Outline each Plasmodium falciparum-infected red blood cell.
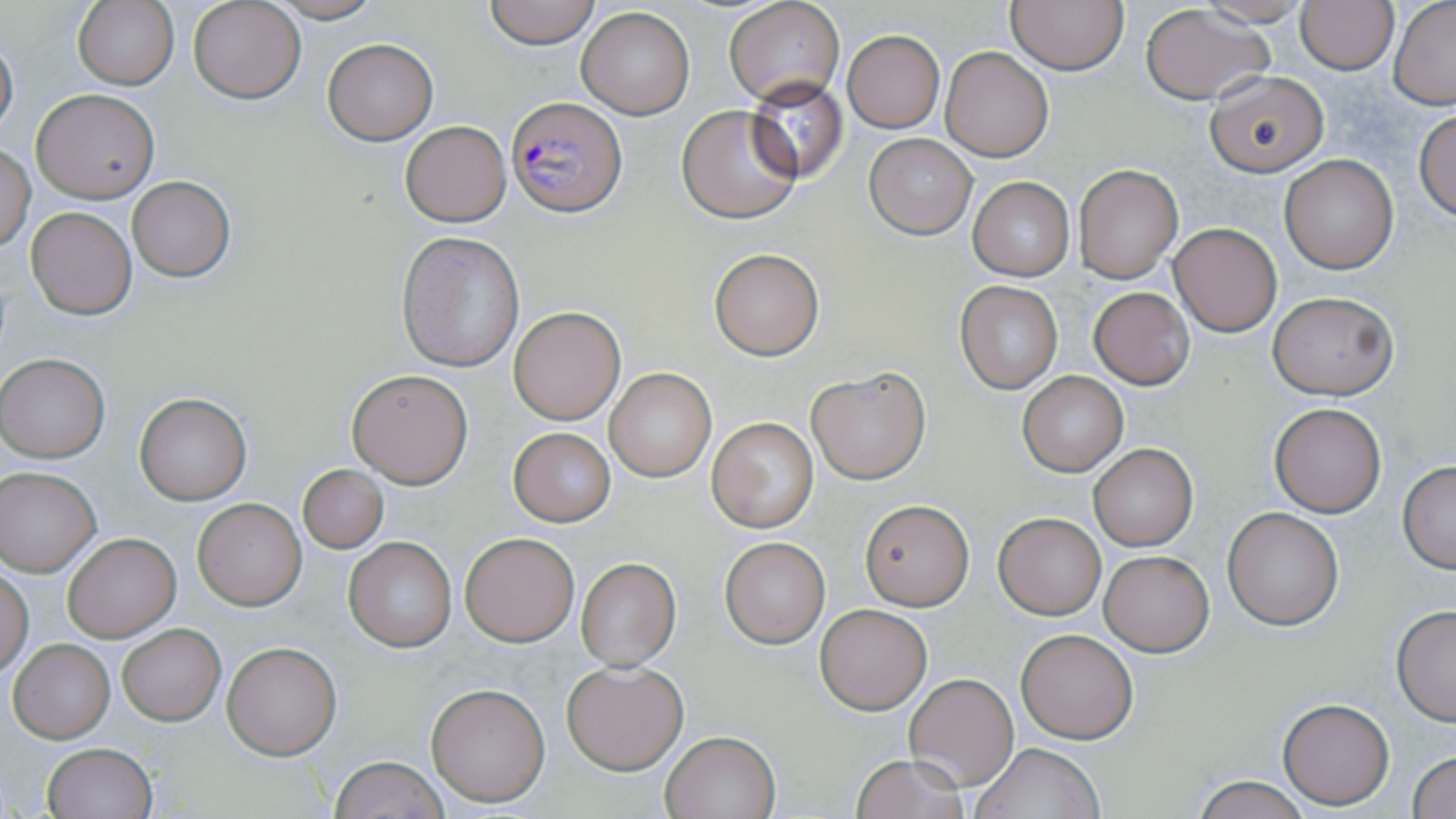

Approximate bounding boxes as (x1,y1)-(x2,y2) corner pairs in pixels.
Plasmodium falciparum-infected red blood cells: (508,96)-(627,217).

Uninfected red blood cell locations: (188,0)-(306,103), (264,0)-(386,23), (484,0)-(600,48), (73,1)-(178,89), (725,1)-(844,106), (1007,1)-(1128,74), (1195,1)-(1313,26), (1295,1)-(1398,74), (1388,1)-(1456,108), (1139,4)-(1274,105), (577,7)-(695,119), (0,31)-(17,137), (842,31)-(945,132), (322,38)-(437,145), (940,46)-(1052,161), (1203,71)-(1331,178), (745,77)-(847,183), (31,89)-(160,202), (677,105)-(801,223), (1414,109)-(1456,221), (400,120)-(511,226), (864,133)-(976,238), (0,145)-(35,253), (1280,155)-(1399,273), (1073,165)-(1183,282), (127,177)-(236,281), (968,177)-(1075,281), (25,207)-(137,320), (1170,223)-(1282,337), (397,232)-(527,373), (709,247)-(824,360), (954,280)-(1065,395), (1089,287)-(1194,388), (1267,290)-(1398,400), (508,307)-(626,425), (1,354)-(109,462), (806,367)-(930,485), (346,368)-(473,488), (605,369)-(716,481), (1018,370)-(1128,475), (134,393)-(251,504), (1269,402)-(1386,517), (706,417)-(818,534), (508,428)-(615,526), (1089,443)-(1197,552), (1397,461)-(1456,573), (298,465)-(388,554), (0,467)-(101,576), (192,498)-(307,610), (859,498)-(976,610), (1222,508)-(1344,629), (994,512)-(1106,619), (460,532)-(580,646), (63,533)-(179,641), (344,537)-(457,651), (719,538)-(830,649), (1099,549)-(1215,657), (574,558)-(680,670), (0,564)-(34,675), (814,604)-(932,714), (1391,605)-(1456,725), (117,624)-(225,725), (1016,628)-(1139,744), (8,638)-(114,742), (223,641)-(343,759), (561,660)-(689,773), (904,673)-(1018,790), (425,681)-(551,806), (1277,697)-(1394,808), (660,729)-(781,818), (42,743)-(157,819), (973,743)-(1104,819), (1408,750)-(1456,818), (851,754)-(971,818), (328,756)-(450,819), (1190,775)-(1314,818). Slide-level diagnosis: Plasmodium falciparum. Single field of view. Light microscopy. May-Grünwald-Giemsa-stained preparation. Image is 1456×819 pixels. Captured at 1000x magnification. Thin blood smear.